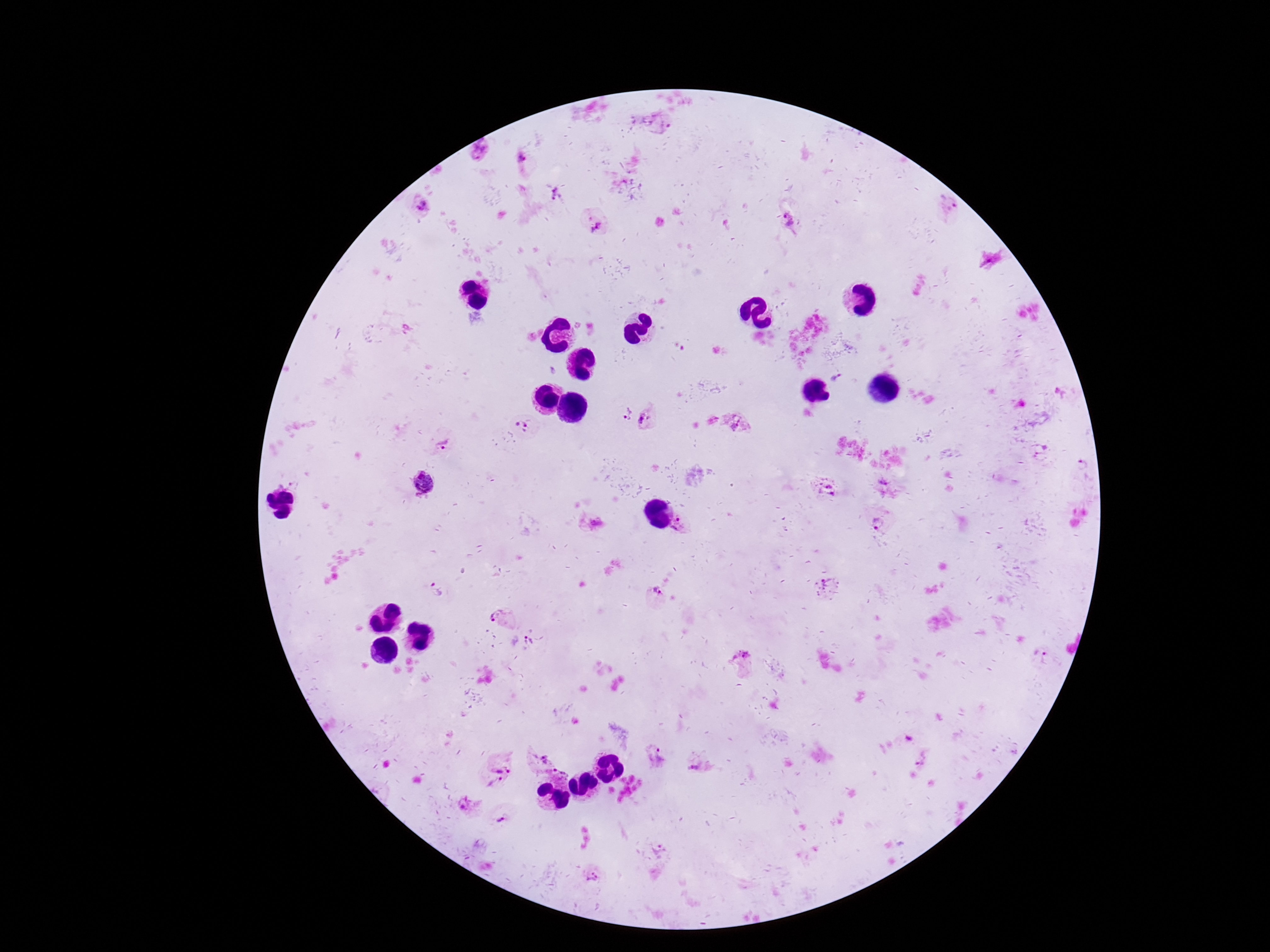

Approximate centers as (x, y) in pixels.
Summary:
  - Plasmodium parasite locations: (663, 123), (480, 150), (524, 161), (557, 193), (421, 205), (949, 205), (789, 219), (594, 225), (836, 378), (625, 412), (646, 419), (522, 423), (737, 424), (443, 442), (1042, 449), (1083, 464), (424, 483), (882, 484), (829, 490), (876, 522), (592, 524), (680, 526), (823, 582), (438, 587), (655, 595), (503, 617), (527, 641), (743, 655), (1043, 659), (908, 737), (543, 754), (502, 756), (924, 756), (658, 757), (699, 769), (559, 779), (496, 784), (470, 806), (504, 820), (660, 849), (592, 875)
  - Image size: 1270×952 pixels
  - Field of view: one from this slide
  - Preparation: thick blood film
  - Magnification: 100x
  - Patient malaria status: positive
  - Stain: Giemsa
  - Capture: smartphone camera through the microscope eyepiece